Mark where platelets are.
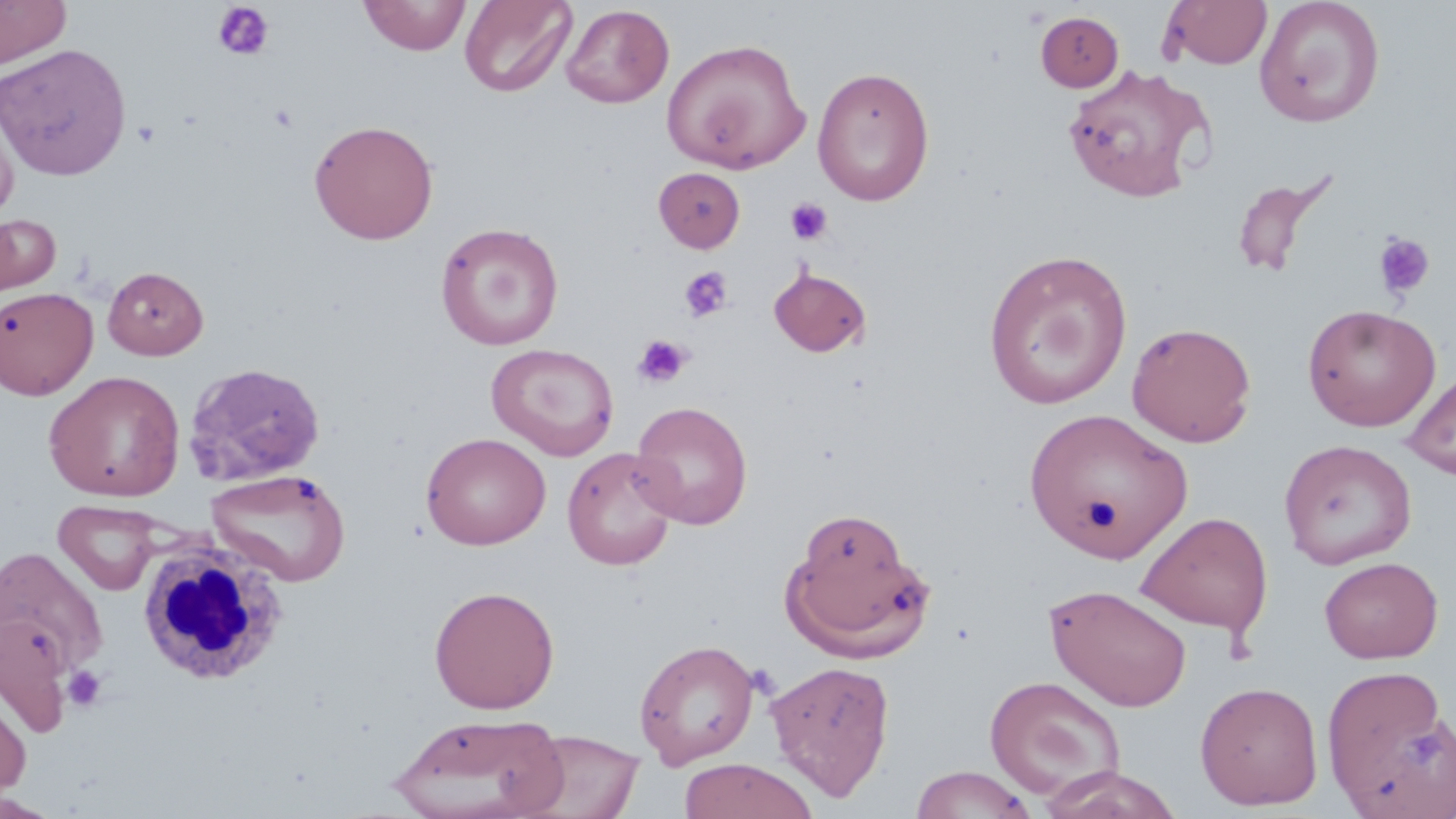
Approximate bounding boxes as (x1, y1, x2, y2) in pixels.
Platelets: (212, 2, 275, 61), (785, 198, 833, 245), (1373, 231, 1435, 300), (679, 267, 733, 323), (633, 334, 691, 389), (61, 665, 107, 713).

Summary:
  - Uninfected red blood cell locations: (0, 0, 71, 68), (360, 0, 470, 55), (459, 0, 577, 98), (1163, 0, 1272, 69), (1254, 0, 1385, 127), (561, 4, 674, 108), (1036, 12, 1123, 91), (662, 38, 810, 174), (0, 43, 132, 180), (1061, 64, 1214, 202), (812, 66, 935, 205), (0, 108, 18, 221), (309, 119, 439, 245), (654, 167, 745, 252), (1231, 171, 1334, 278), (0, 213, 61, 300), (435, 221, 564, 351), (984, 249, 1132, 409), (103, 265, 208, 360), (769, 266, 871, 357), (0, 286, 98, 400), (1302, 303, 1441, 431), (1127, 321, 1257, 447), (486, 343, 619, 460), (184, 362, 326, 486), (1402, 369, 1456, 481), (44, 370, 186, 501), (631, 401, 752, 529), (1024, 407, 1193, 562), (421, 432, 550, 550), (1279, 439, 1417, 569), (562, 447, 681, 570), (207, 468, 350, 586), (53, 499, 165, 596), (785, 511, 932, 662), (1136, 511, 1273, 637), (1, 547, 109, 674), (1319, 556, 1443, 663), (1043, 583, 1193, 712), (429, 585, 560, 713), (1, 613, 74, 737), (633, 638, 760, 768), (630, 649, 895, 778), (766, 660, 895, 801), (1321, 663, 1456, 818), (984, 674, 1126, 802), (1194, 680, 1324, 810), (0, 684, 32, 803), (389, 712, 568, 818), (517, 729, 646, 819), (678, 758, 818, 819), (910, 765, 1038, 819), (1036, 765, 1186, 819), (0, 792, 64, 819)
  - White blood cell locations: (134, 532, 290, 687)
  - Slide-level diagnosis: no evidence of blood parasites
  - Field of view: single
  - Image size: 1456×819 pixels
  - Preparation: thin blood smear
  - Magnification: 1000x
  - Stain: May-Grünwald-Giemsa
  - Modality: light microscopy